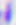

magnification = 400x
identification = Toxoplasma gondii
modality = photomicrograph